Give the position of every Plasmodium parasite.
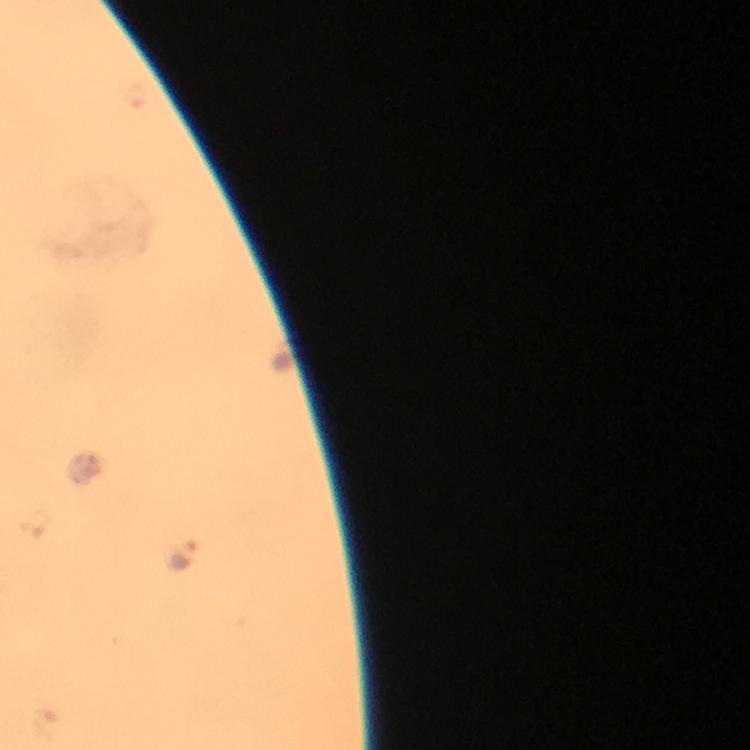
Approximate centers as (x, y) in pixels.
Plasmodium parasites: (180, 557).

100x magnification. Image is 750×750 pixels. From a diagnostic examination for malaria. Cropped region of a single field of view. Thick blood smear. Immersion oil applied. Photographed with a smartphone mounted on the microscope. Giemsa-stained preparation.